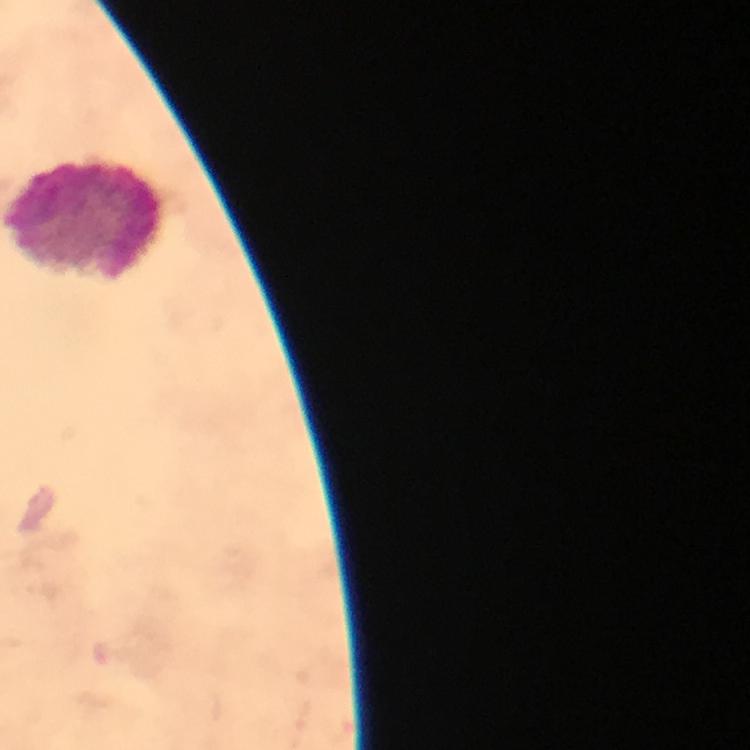
Approximate object centers, in pixels from the top-left corner.
Summary:
  - Leukocyte locations: (x=85, y=218)
  - Malaria parasites: none detected
  - Magnification: 100x
  - Preparation: thick blood smear
  - Stain: Giemsa
  - Cropped from: a single field of view
  - Context: from a diagnostic examination for malaria
  - Immersion oil: used
  - Capture: smartphone mounted on the microscope
  - Image size: 750×750 pixels